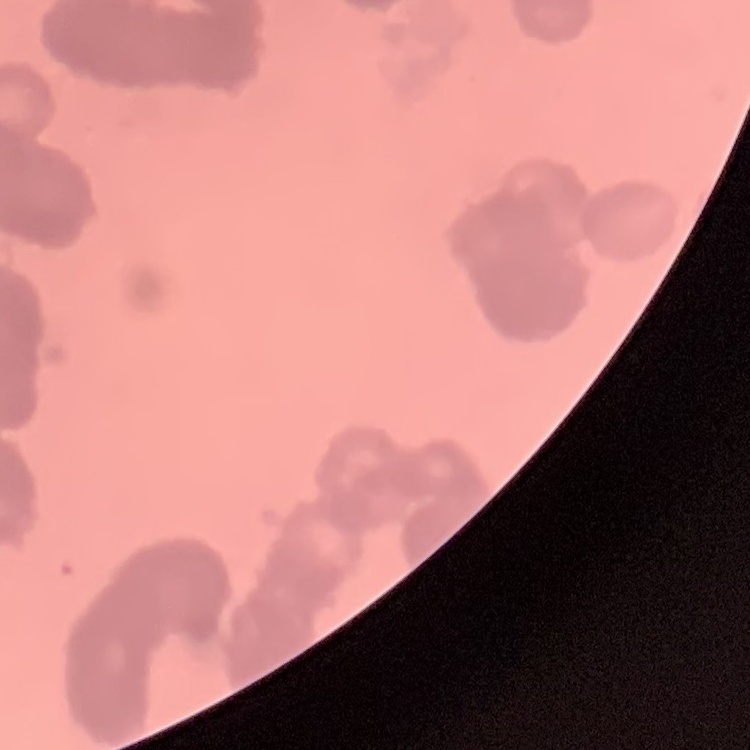
Summary:
  - Red blood cell morphology: rouleaux formation
  - Stain: Field's or Giemsa
  - Preparation: thin peripheral smear
  - Image type: square crop of a larger photomicrograph